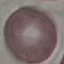
Malaria status: uninfected. Thin smear of blood. Acquired by smartphone through the microscope eyepiece. Giemsa-stained preparation. Cell patch, automatically extracted from a larger field of view and resized to 64 × 64 pixels.